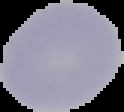
Cell region segmented out of the field of view; the surrounding area is masked to black. From a thin blood smear. Image is 124×112 pixels. Malaria status: uninfected.